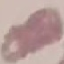

Summary:
  - Result: no malaria parasites seen
  - Preparation: thin smear
  - Image type: automatically extracted cell patch, resized to 64 × 64 pixels
  - Stain: Giemsa
  - Capture: smartphone camera at the microscope eyepiece